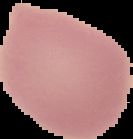
preparation = thin blood film
image size = 133×139 pixels
result = negative for malaria parasites
image type = segmented cell region with the area outside set to black